Locate every malaria parasite.
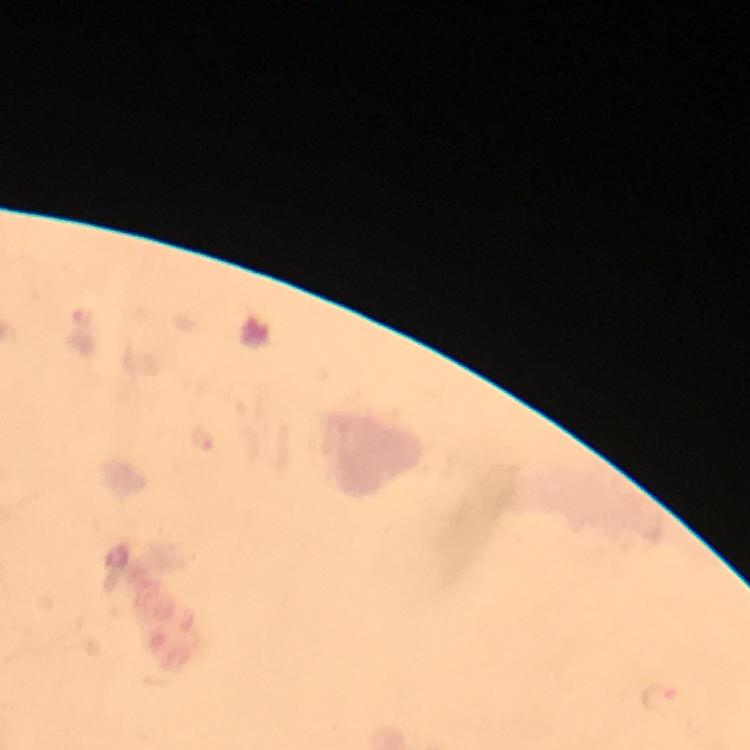
Approximate centers as (x, y) in pixels.
Malaria parasites: (661, 699).

Summary:
  - Cropped from: a single field of view
  - Context: from a diagnostic examination for malaria
  - Magnification: 100x
  - Stain: Giemsa
  - Capture: smartphone camera through the microscope
  - Immersion oil: applied
  - Preparation: thick blood film
  - Image size: 750×750 pixels